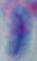

Summary:
  - Magnification: 1000x
  - Modality: micrograph
  - Identification: Toxoplasma gondii